Classify this cell by malaria status.
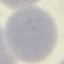

It is uninfected.

stain = Giemsa
image type = automatically extracted cell patch, resized to 64 × 64 pixels
capture = smartphone camera at the microscope eyepiece
preparation = thin smear